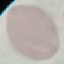
malaria status = uninfected
stain = Giemsa
preparation = thin smear
image type = cell patch, automatically extracted from a larger field of view and resized to 64 × 64 pixels
capture = smartphone through the microscope eyepiece